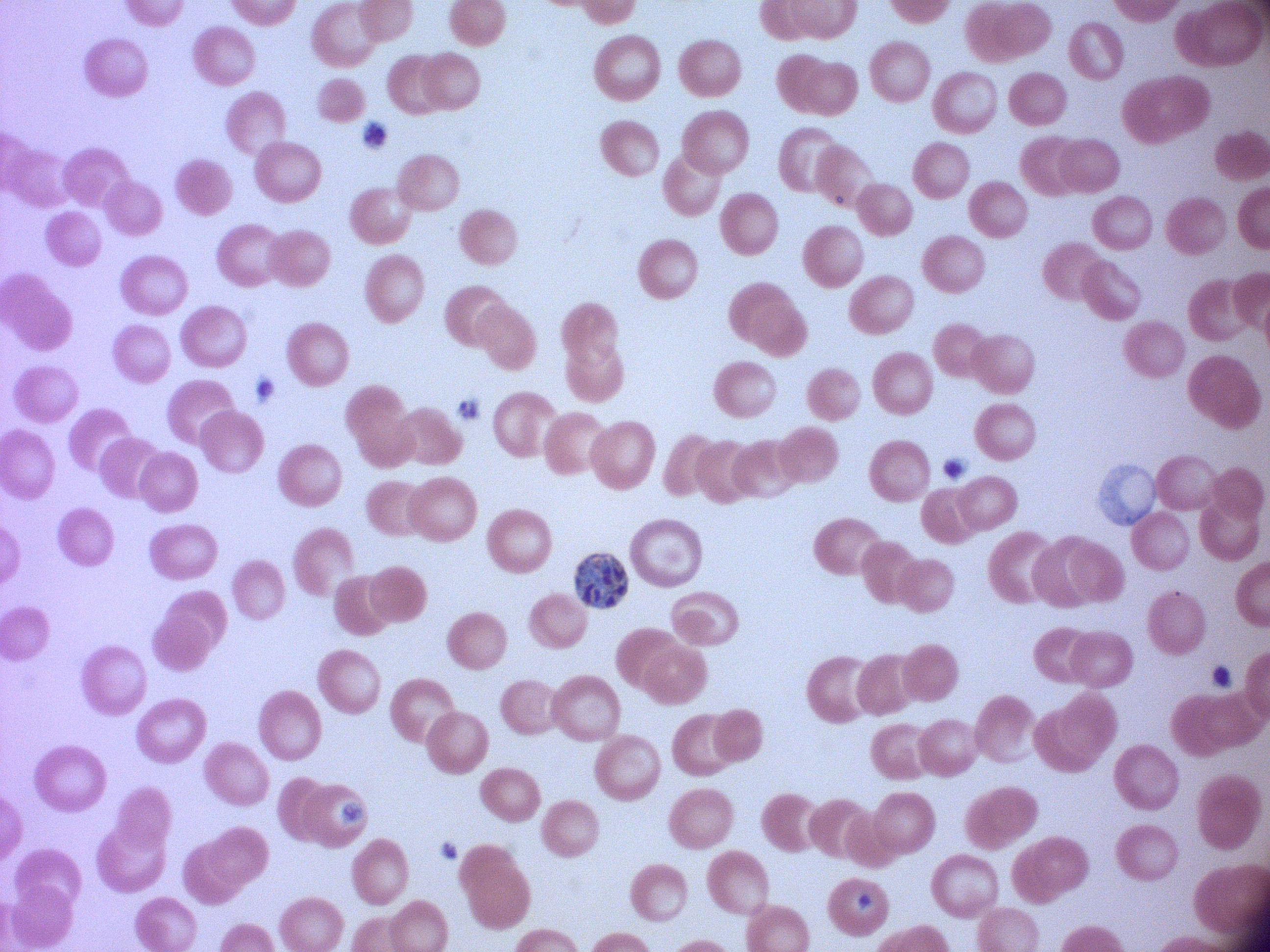

{
  "magnification": "100x",
  "microscope": "Leica DM2000 with built-in camera",
  "image_size": "1270×952 pixels",
  "stain": "Giemsa",
  "preparation": "thin blood film",
  "field_of_view": "one from this slide",
  "species": "Plasmodium falciparum",
  "schizont_locations": "approximate bounding boxes as (x1, y1, x2, y2) in pixels, from the source annotation, which is not necessarily exhaustive: (574, 553, 628, 609)"
}